State the blood parasite species.
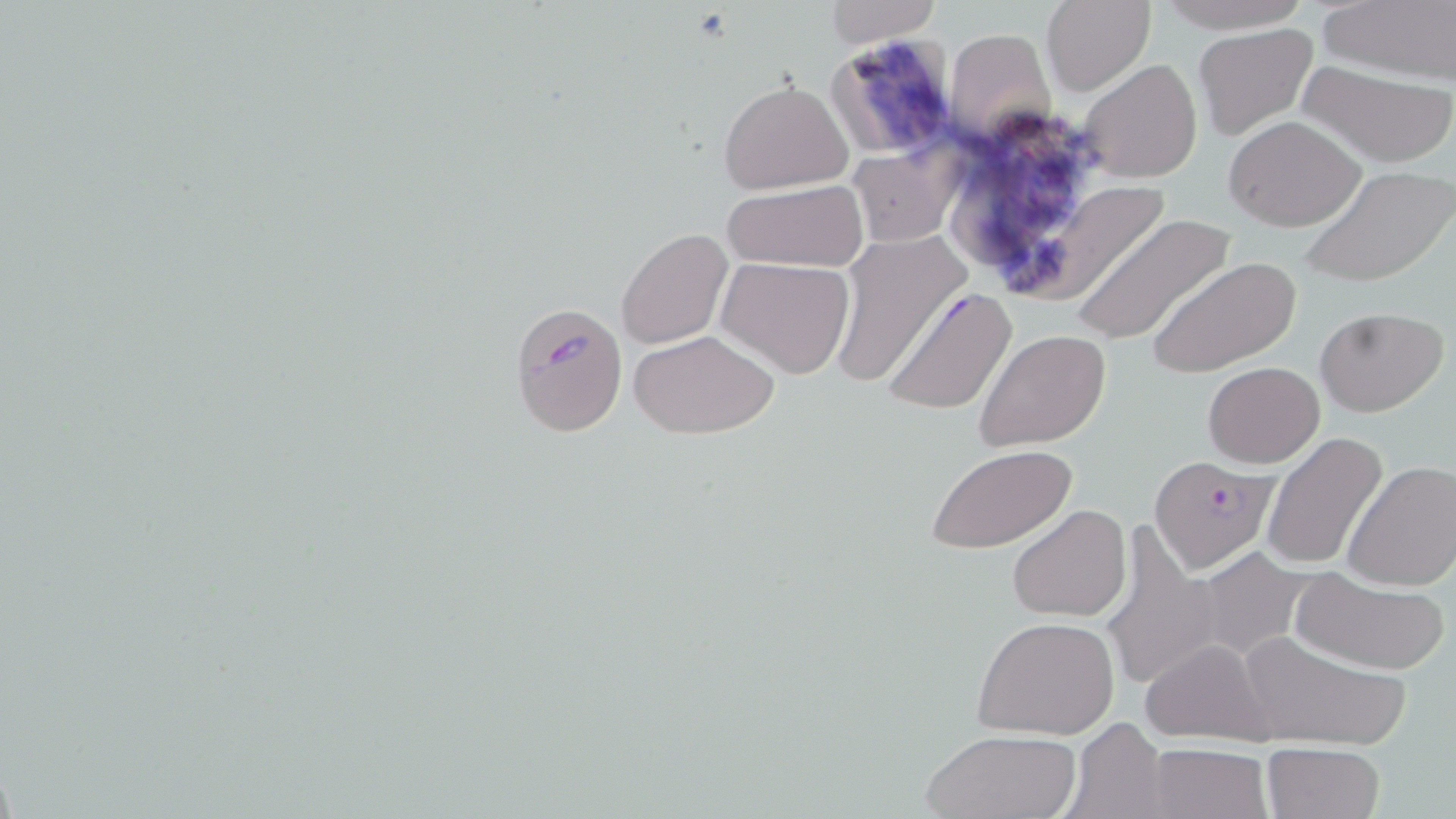

Plasmodium falciparum.

Summary:
  - Coordinate format: approximate bounding boxes as (x1, y1, x2, y2) in pixels
  - Uninfected red blood cell locations: (1158, 0, 1307, 31), (824, 1, 940, 47), (1042, 1, 1154, 95), (1319, 1, 1456, 84), (1194, 24, 1319, 139), (942, 28, 1051, 143), (1293, 58, 1456, 168), (1077, 59, 1203, 185), (718, 77, 853, 195), (1225, 116, 1366, 232), (963, 123, 1079, 257), (845, 145, 959, 248), (1300, 164, 1456, 289), (718, 182, 868, 273), (1024, 184, 1169, 296), (1071, 214, 1237, 346), (615, 227, 733, 351), (825, 233, 970, 389), (717, 256, 856, 378), (1149, 256, 1300, 377), (880, 286, 1018, 417), (1316, 306, 1447, 417), (630, 329, 778, 439), (973, 329, 1112, 450), (1202, 361, 1324, 467), (1262, 431, 1388, 571), (925, 443, 1078, 554), (1340, 460, 1456, 591), (1007, 502, 1131, 621), (1098, 526, 1230, 697), (1290, 568, 1453, 675), (972, 615, 1120, 740), (1235, 630, 1410, 749), (1138, 639, 1278, 746), (1065, 718, 1169, 818), (920, 728, 1081, 818), (1146, 743, 1272, 819), (1261, 743, 1384, 819)
  - Plasmodium falciparum-infected red blood cell locations: (511, 303, 628, 435), (1148, 456, 1280, 572)
  - Image size: 1456×819 pixels
  - Stain: May-Grünwald-Giemsa
  - Modality: optical microscopy
  - Preparation: thin blood film
  - Field of view: single
  - Magnification: 1000x